Assess the morphology of the red blood cells.
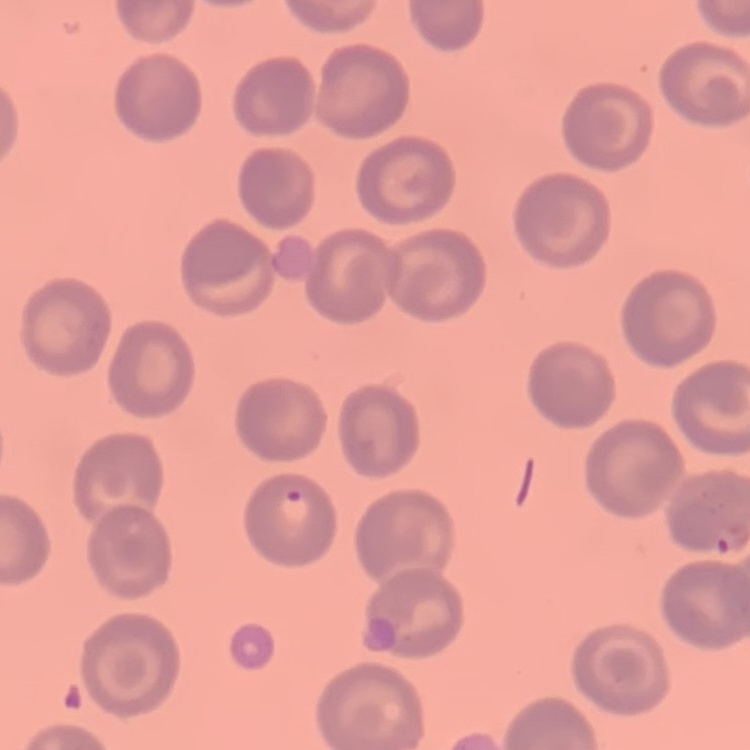

No rouleaux formation.

Summary:
  - Image type: one tile cut from a larger photomicrograph
  - Stain: Field's or Giemsa
  - Preparation: thin blood film